Classify this cell by malaria status.
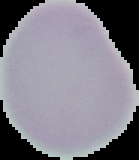
It is uninfected.

{
  "preparation": "thin blood film",
  "image_size": "139×160 pixels",
  "image_type": "cell region segmented out of the field of view; surrounding area masked to black"
}